Classify this cell by malaria status.
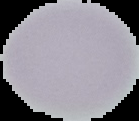

It is uninfected.

Segmented cell region on a black background. Image is 139×121 pixels. From a thin blood film.